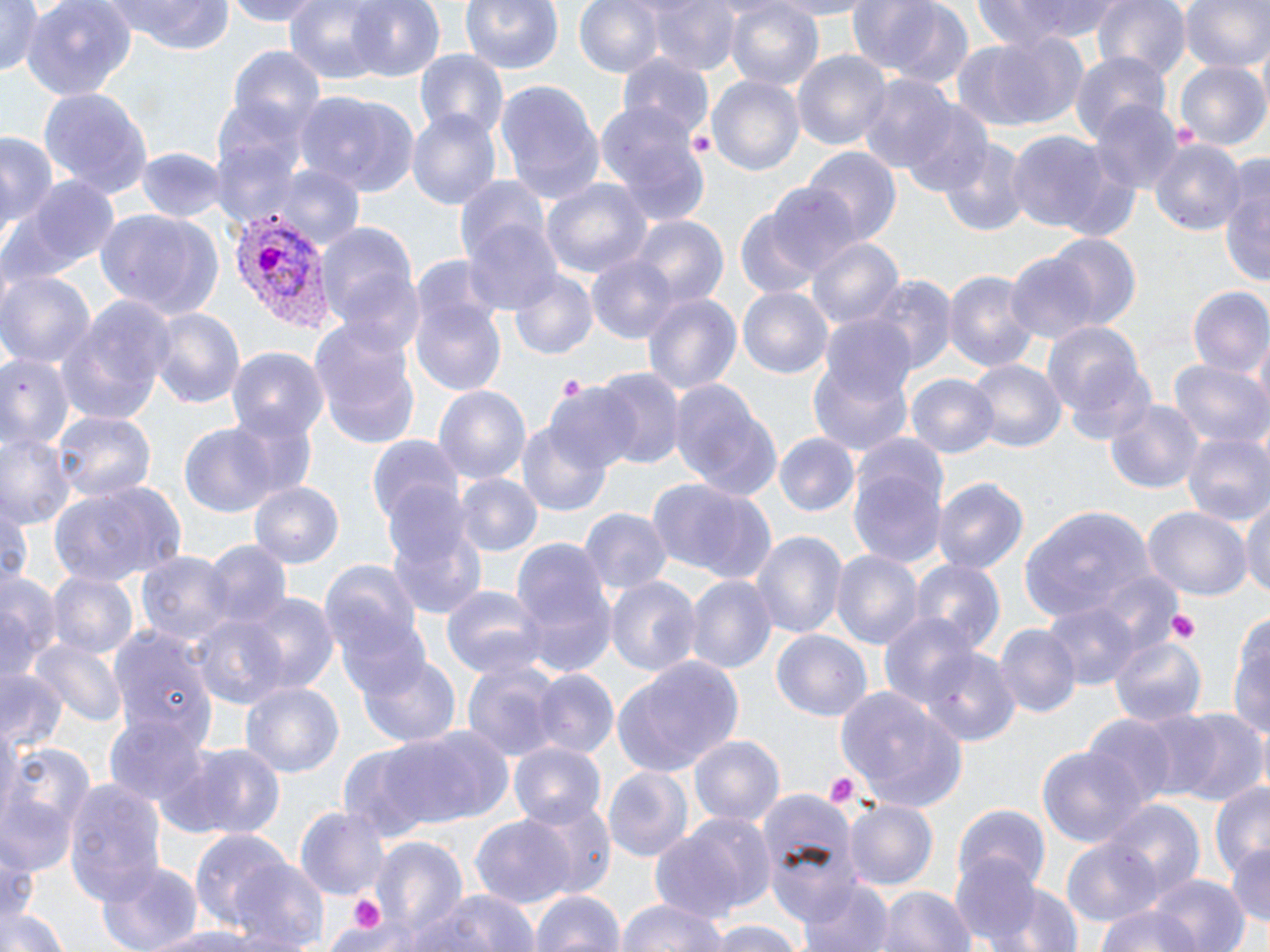

Approximate bounding boxes as named x1/y1/x2/y2 corners in pixels. Platelet locations: (x1=557, y1=373, x2=586, y2=402), (x1=1166, y1=607, x2=1201, y2=642), (x1=826, y1=773, x2=858, y2=808), (x1=344, y1=892, x2=390, y2=937). Uninfected red blood cell locations: (x1=0, y1=0, x2=50, y2=75), (x1=106, y1=0, x2=236, y2=55), (x1=218, y1=0, x2=330, y2=25), (x1=282, y1=0, x2=396, y2=83), (x1=345, y1=0, x2=446, y2=84), (x1=459, y1=0, x2=566, y2=73), (x1=573, y1=0, x2=668, y2=79), (x1=646, y1=0, x2=739, y2=77), (x1=762, y1=0, x2=880, y2=17), (x1=845, y1=0, x2=971, y2=85), (x1=972, y1=0, x2=1123, y2=49), (x1=1091, y1=0, x2=1191, y2=80), (x1=1178, y1=0, x2=1269, y2=74), (x1=23, y1=1, x2=136, y2=98), (x1=723, y1=1, x2=825, y2=93), (x1=958, y1=32, x2=1090, y2=131), (x1=231, y1=48, x2=326, y2=137), (x1=415, y1=50, x2=509, y2=142), (x1=792, y1=50, x2=891, y2=150), (x1=1071, y1=52, x2=1171, y2=146), (x1=614, y1=55, x2=716, y2=146), (x1=1175, y1=60, x2=1268, y2=151), (x1=708, y1=75, x2=804, y2=177), (x1=862, y1=76, x2=958, y2=173), (x1=495, y1=79, x2=604, y2=202), (x1=39, y1=86, x2=154, y2=198), (x1=210, y1=92, x2=316, y2=215), (x1=297, y1=92, x2=421, y2=197), (x1=1089, y1=101, x2=1181, y2=196), (x1=899, y1=104, x2=995, y2=199), (x1=598, y1=107, x2=711, y2=225), (x1=407, y1=110, x2=500, y2=208), (x1=1005, y1=132, x2=1120, y2=236), (x1=0, y1=134, x2=57, y2=231), (x1=1150, y1=137, x2=1246, y2=239), (x1=936, y1=138, x2=1030, y2=235), (x1=137, y1=146, x2=226, y2=220), (x1=801, y1=146, x2=903, y2=249), (x1=275, y1=163, x2=364, y2=250), (x1=1221, y1=165, x2=1270, y2=296), (x1=454, y1=173, x2=552, y2=272), (x1=7, y1=175, x2=116, y2=284), (x1=540, y1=177, x2=653, y2=287), (x1=769, y1=184, x2=862, y2=282), (x1=735, y1=206, x2=827, y2=298), (x1=93, y1=207, x2=224, y2=320), (x1=626, y1=216, x2=728, y2=309), (x1=313, y1=217, x2=421, y2=337), (x1=462, y1=217, x2=564, y2=317), (x1=1043, y1=233, x2=1142, y2=332), (x1=804, y1=235, x2=907, y2=332), (x1=1003, y1=251, x2=1103, y2=346), (x1=586, y1=253, x2=679, y2=345), (x1=945, y1=268, x2=1038, y2=374), (x1=0, y1=269, x2=96, y2=369), (x1=509, y1=271, x2=598, y2=360), (x1=868, y1=276, x2=956, y2=378), (x1=737, y1=284, x2=832, y2=377), (x1=1186, y1=286, x2=1270, y2=380), (x1=412, y1=290, x2=509, y2=400), (x1=641, y1=290, x2=742, y2=400), (x1=57, y1=301, x2=172, y2=423), (x1=148, y1=306, x2=245, y2=413), (x1=820, y1=314, x2=919, y2=408), (x1=309, y1=316, x2=422, y2=451), (x1=1043, y1=326, x2=1155, y2=442), (x1=0, y1=348, x2=75, y2=458), (x1=228, y1=348, x2=327, y2=444), (x1=806, y1=356, x2=914, y2=456), (x1=963, y1=358, x2=1068, y2=456), (x1=1169, y1=358, x2=1270, y2=450), (x1=595, y1=366, x2=684, y2=470), (x1=906, y1=372, x2=1001, y2=460), (x1=666, y1=378, x2=782, y2=505), (x1=433, y1=386, x2=531, y2=489), (x1=548, y1=386, x2=639, y2=475), (x1=1105, y1=398, x2=1204, y2=493), (x1=224, y1=410, x2=321, y2=502), (x1=52, y1=411, x2=154, y2=506), (x1=516, y1=420, x2=609, y2=515), (x1=176, y1=422, x2=286, y2=520), (x1=0, y1=431, x2=74, y2=527), (x1=773, y1=432, x2=859, y2=517), (x1=1182, y1=432, x2=1270, y2=528), (x1=368, y1=433, x2=465, y2=539), (x1=848, y1=446, x2=946, y2=572), (x1=455, y1=473, x2=543, y2=558), (x1=646, y1=477, x2=779, y2=584), (x1=933, y1=478, x2=1028, y2=577), (x1=48, y1=479, x2=187, y2=585), (x1=248, y1=481, x2=342, y2=567), (x1=1243, y1=496, x2=1270, y2=601), (x1=0, y1=503, x2=31, y2=585), (x1=1020, y1=506, x2=1153, y2=621), (x1=580, y1=508, x2=672, y2=597), (x1=1143, y1=509, x2=1250, y2=601), (x1=384, y1=510, x2=491, y2=623), (x1=750, y1=530, x2=845, y2=642), (x1=510, y1=535, x2=615, y2=652), (x1=202, y1=540, x2=293, y2=631), (x1=833, y1=550, x2=923, y2=653), (x1=137, y1=552, x2=232, y2=648), (x1=319, y1=559, x2=425, y2=663), (x1=912, y1=561, x2=1006, y2=660), (x1=0, y1=569, x2=60, y2=680), (x1=1089, y1=571, x2=1185, y2=659), (x1=47, y1=572, x2=138, y2=661), (x1=686, y1=576, x2=775, y2=674), (x1=606, y1=577, x2=700, y2=676), (x1=441, y1=586, x2=546, y2=677), (x1=243, y1=592, x2=339, y2=697), (x1=332, y1=593, x2=431, y2=699), (x1=1043, y1=600, x2=1138, y2=694), (x1=1231, y1=606, x2=1270, y2=750), (x1=191, y1=611, x2=294, y2=713), (x1=879, y1=614, x2=980, y2=709), (x1=107, y1=625, x2=217, y2=753), (x1=995, y1=625, x2=1079, y2=721), (x1=772, y1=630, x2=873, y2=722), (x1=1106, y1=635, x2=1206, y2=727), (x1=31, y1=638, x2=127, y2=728), (x1=920, y1=649, x2=1021, y2=746), (x1=356, y1=654, x2=462, y2=750), (x1=611, y1=656, x2=744, y2=777), (x1=463, y1=661, x2=560, y2=761), (x1=530, y1=669, x2=618, y2=759), (x1=0, y1=670, x2=68, y2=754), (x1=240, y1=681, x2=344, y2=778), (x1=835, y1=687, x2=969, y2=809), (x1=1135, y1=708, x2=1228, y2=800), (x1=1169, y1=708, x2=1269, y2=808), (x1=1085, y1=714, x2=1178, y2=805), (x1=105, y1=718, x2=208, y2=810), (x1=383, y1=727, x2=515, y2=829), (x1=689, y1=734, x2=785, y2=830), (x1=336, y1=739, x2=467, y2=842), (x1=510, y1=741, x2=607, y2=827), (x1=176, y1=743, x2=289, y2=841), (x1=2, y1=745, x2=91, y2=867), (x1=1036, y1=745, x2=1146, y2=847), (x1=604, y1=767, x2=695, y2=861), (x1=65, y1=778, x2=169, y2=904), (x1=1208, y1=779, x2=1269, y2=880), (x1=1, y1=794, x2=75, y2=883), (x1=761, y1=795, x2=860, y2=921), (x1=521, y1=798, x2=619, y2=900), (x1=843, y1=799, x2=937, y2=891), (x1=1103, y1=800, x2=1206, y2=904), (x1=295, y1=804, x2=391, y2=901), (x1=955, y1=805, x2=1051, y2=895), (x1=653, y1=810, x2=773, y2=934), (x1=471, y1=815, x2=575, y2=909), (x1=186, y1=827, x2=302, y2=933), (x1=370, y1=835, x2=468, y2=941), (x1=1059, y1=835, x2=1164, y2=928), (x1=1227, y1=843, x2=1270, y2=930), (x1=952, y1=851, x2=1044, y2=948), (x1=95, y1=859, x2=204, y2=952), (x1=229, y1=859, x2=332, y2=952), (x1=1144, y1=874, x2=1248, y2=952), (x1=798, y1=878, x2=894, y2=952), (x1=990, y1=881, x2=1085, y2=952), (x1=875, y1=886, x2=974, y2=952), (x1=527, y1=889, x2=628, y2=952), (x1=403, y1=890, x2=539, y2=952), (x1=616, y1=897, x2=732, y2=952), (x1=1, y1=904, x2=71, y2=952), (x1=1098, y1=905, x2=1204, y2=952), (x1=703, y1=921, x2=808, y2=952), (x1=134, y1=925, x2=267, y2=951). Plasmodium vivax-infected red blood cell locations: (x1=229, y1=211, x2=331, y2=330). Slide-level diagnosis: Plasmodium vivax. May-Grünwald-Giemsa-stained preparation. Image is 1270×952 pixels. Optical microscopy. Captured at 1000x magnification. Thin blood film. Single field of view.